Outline each blood parasite and name the species.
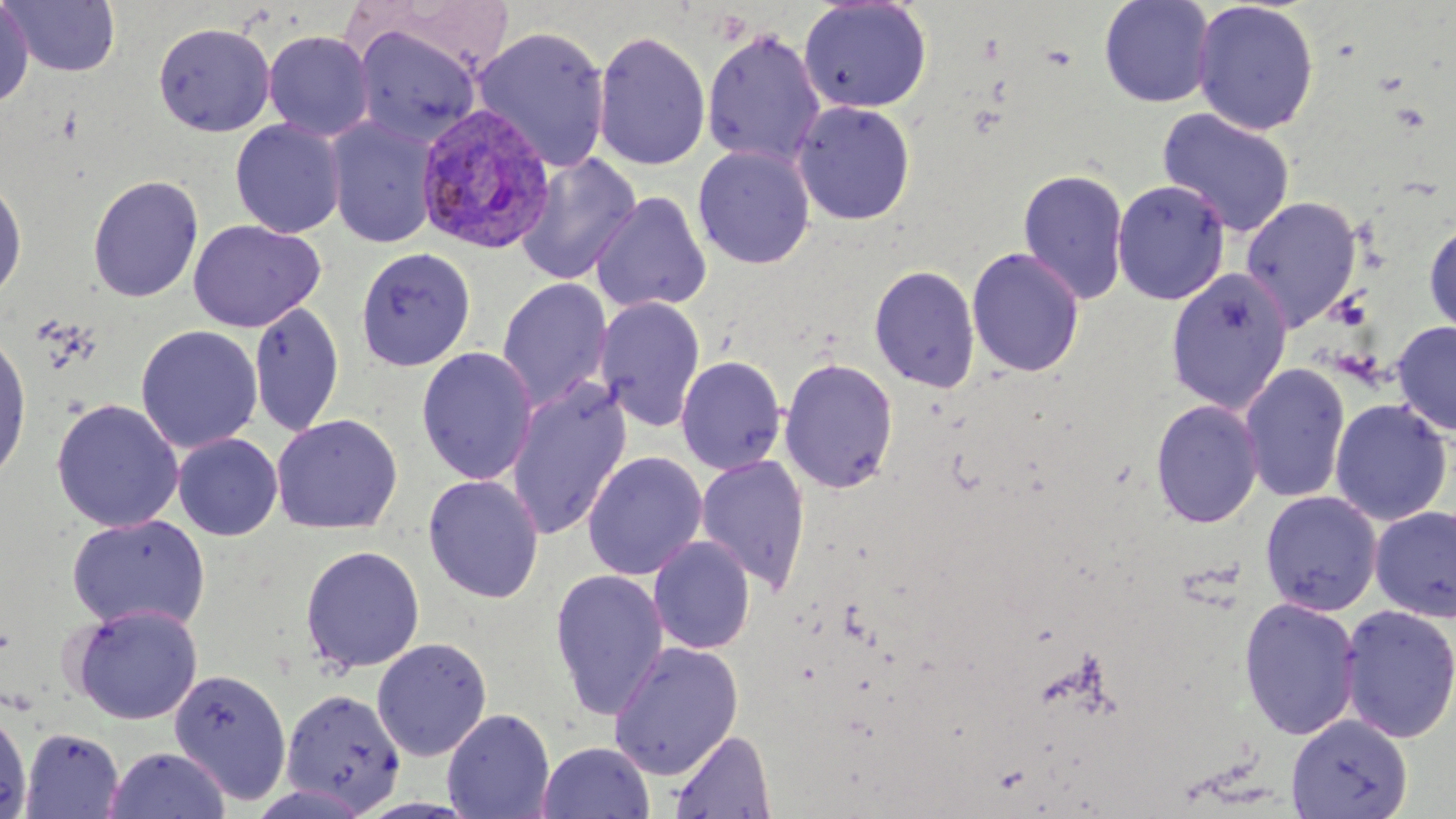
Approximate bounding boxes as (x1,y1)-(x2,y2) corner pairs in pixels.
Plasmodium vivax-infected red blood cells: (416,103)-(557,256).
No Plasmodium falciparum, Plasmodium ovale, Plasmodium malariae, Babesia divergens, or Trypanosoma brucei observed.

Uninfected red blood cell locations: (2,0)-(121,77), (1098,0)-(1215,107), (798,1)-(933,113), (1192,1)-(1320,136), (0,3)-(34,108), (153,21)-(275,137), (352,26)-(482,147), (472,26)-(611,172), (701,26)-(826,167), (263,30)-(375,141), (593,30)-(711,172), (792,100)-(916,226), (1156,108)-(1296,239), (326,116)-(439,249), (229,119)-(346,239), (693,145)-(815,269), (515,153)-(642,286), (1018,167)-(1129,306), (87,174)-(204,303), (0,175)-(28,303), (1112,180)-(1230,306), (591,191)-(712,315), (1240,196)-(1363,330), (1424,216)-(1456,339), (188,218)-(325,333), (355,247)-(476,370), (967,247)-(1085,379), (869,264)-(981,394), (1165,266)-(1294,414), (496,277)-(612,411), (595,296)-(706,433), (248,300)-(345,437), (1392,321)-(1456,436), (135,325)-(263,454), (0,330)-(32,489), (416,346)-(539,485), (676,355)-(786,475), (779,357)-(899,494), (1239,362)-(1351,504), (506,377)-(632,541), (51,398)-(184,532), (1150,398)-(1264,529), (1329,399)-(1453,526), (271,414)-(403,535), (172,433)-(283,541), (583,451)-(707,581), (695,454)-(811,593), (423,474)-(545,604), (1259,490)-(1383,616), (1369,505)-(1456,623), (67,514)-(211,633), (648,536)-(756,654), (300,545)-(425,673), (550,568)-(669,720), (1238,596)-(1362,741), (69,604)-(203,725), (1339,604)-(1456,744), (371,637)-(492,761), (607,640)-(744,780), (168,667)-(293,805), (280,688)-(406,813), (0,706)-(33,818), (442,708)-(555,819), (1287,714)-(1413,819), (19,727)-(125,819), (668,729)-(777,819), (537,741)-(655,819), (104,746)-(231,819). Slide-level diagnosis: Plasmodium vivax. May-Grünwald-Giemsa stain. Light microscopy. Image is 1456×819 pixels. Thin blood smear. Single field of view. 1000x magnification.